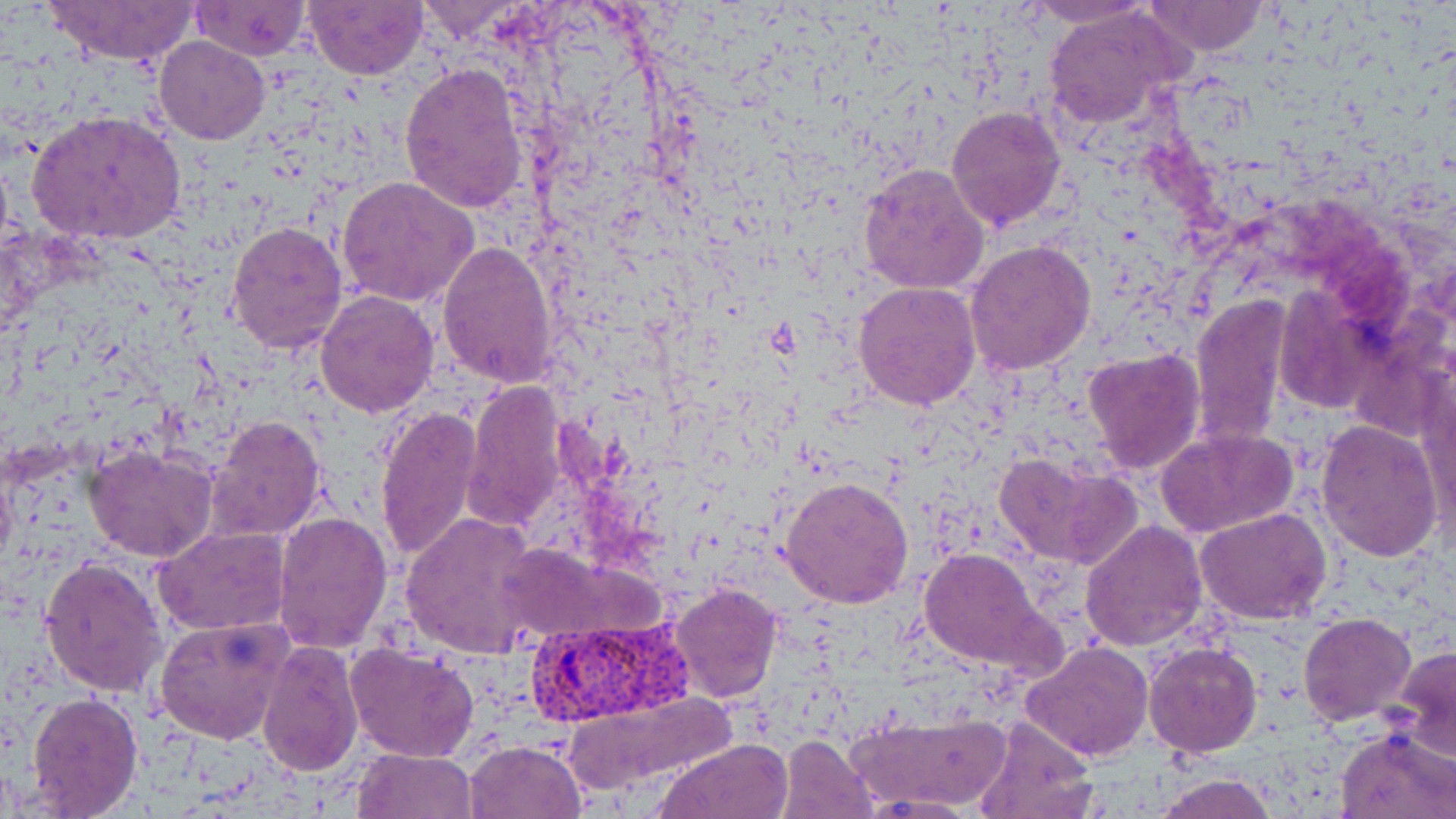
Approximate bounding boxes as (x1, y1, x2, y2) in pixels. Uninfected red blood cell locations: (43, 0, 202, 67), (304, 0, 427, 79), (1025, 0, 1157, 30), (1145, 0, 1270, 56), (189, 1, 310, 62), (413, 1, 526, 44), (1043, 9, 1191, 131), (155, 37, 269, 144), (399, 63, 528, 213), (944, 104, 1067, 231), (26, 109, 187, 245), (857, 161, 991, 298), (336, 175, 478, 307), (226, 219, 348, 357), (964, 239, 1096, 377), (436, 240, 559, 386), (853, 282, 983, 411), (1269, 288, 1379, 420), (314, 289, 440, 417), (1190, 294, 1293, 448), (1082, 348, 1206, 475), (1417, 374, 1456, 542), (461, 381, 569, 532), (375, 405, 482, 564), (205, 416, 328, 540), (1314, 420, 1444, 561), (1154, 427, 1301, 538), (84, 446, 219, 563), (991, 449, 1141, 569), (781, 477, 914, 609), (1195, 507, 1333, 623), (274, 511, 392, 653), (401, 512, 542, 657), (1079, 519, 1207, 651), (154, 526, 291, 635), (917, 547, 1060, 676), (39, 557, 167, 698), (668, 582, 783, 703), (1299, 613, 1416, 726), (154, 617, 295, 745), (258, 638, 364, 776), (1020, 640, 1153, 764), (1144, 641, 1262, 759), (345, 642, 479, 764), (1394, 645, 1456, 760), (24, 690, 143, 816), (555, 691, 740, 799), (855, 711, 1007, 807), (970, 715, 1099, 819), (1336, 726, 1456, 818), (777, 734, 880, 818), (655, 738, 796, 819), (464, 740, 587, 819), (352, 747, 476, 819), (1149, 774, 1279, 819), (862, 792, 981, 816). Plasmodium vivax-infected red blood cell locations: (525, 616, 696, 731). Slide-level diagnosis: Plasmodium vivax. Thin blood smear. 1000x magnification. One field of a larger specimen. Light microscopy. Image is 1456×819 pixels. May-Grünwald-Giemsa stain.